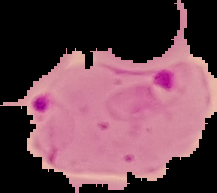
Summary:
  - Image type: cell region segmented out of the field of view; surrounding area masked to black
  - Preparation: thin blood film
  - Malaria status: parasitized
  - Image size: 217×193 pixels